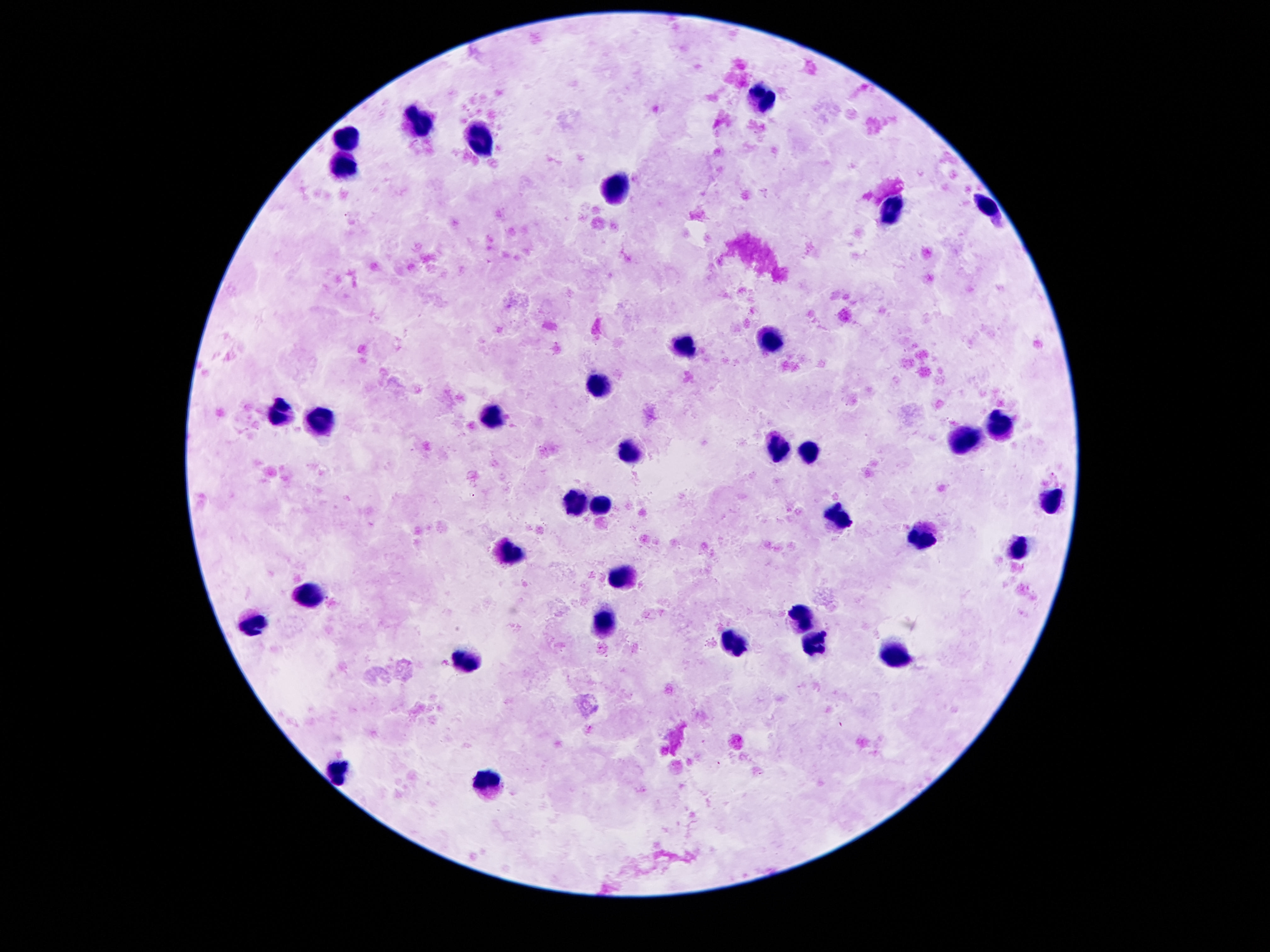 Approximate centers as {x, y} in pixels. Leukocyte locations: {760, 92}, {422, 124}, {350, 137}, {481, 137}, {342, 167}, {613, 190}, {988, 206}, {889, 208}, {768, 344}, {688, 346}, {600, 383}, {281, 413}, {492, 416}, {318, 418}, {998, 422}, {963, 440}, {633, 450}, {781, 450}, {807, 454}, {1051, 498}, {604, 500}, {574, 504}, {840, 518}, {926, 536}, {512, 553}, {621, 577}, {314, 592}, {803, 618}, {252, 619}, {604, 623}, {732, 643}, {815, 647}, {899, 657}, {469, 660}, {338, 770}, {486, 780}. One field from this slide. Photographed through the microscope eyepiece with a smartphone camera. Giemsa-stained preparation. Image is 1270×952 pixels. Thick peripheral-blood smear. Patient malaria status: uninfected. 100x magnification.